Locate every malaria parasite and identify its life-cycle stage.
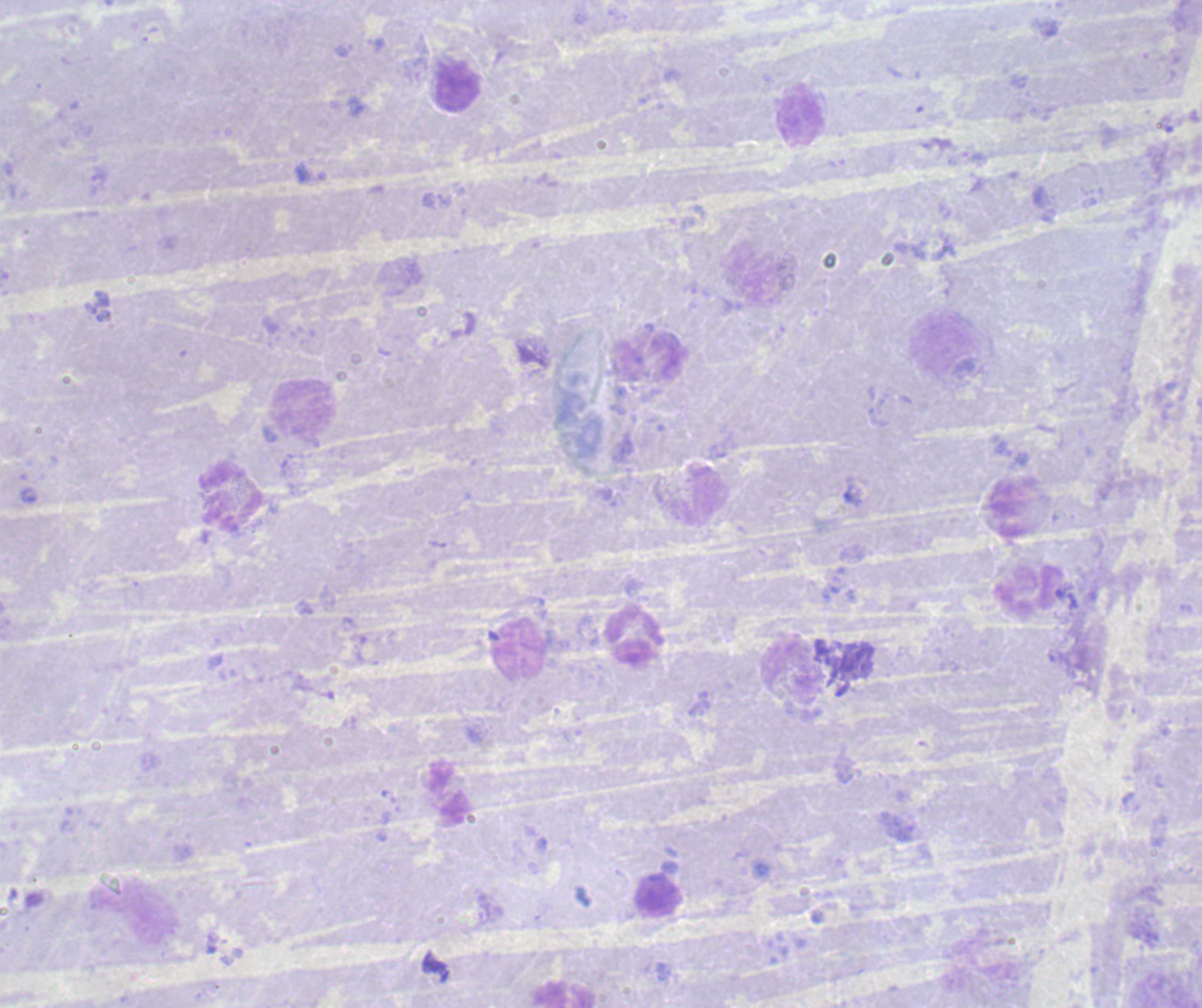
Negative for malaria parasites.

Approximate centers as (x, y) in pixels. Leukocyte locations: (457, 86), (799, 115), (305, 410), (1031, 595), (634, 637), (518, 649), (792, 671), (565, 995). Romanowsky stain. Thick blood film. Image is 1202×1008 pixels. Single field of view. 100x magnification. Background quality: poor. Previously used in a real diagnosis.